Name the cell type shown.
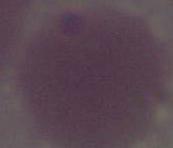
An erythrocyte.

magnification = 1000x
modality = photomicrograph